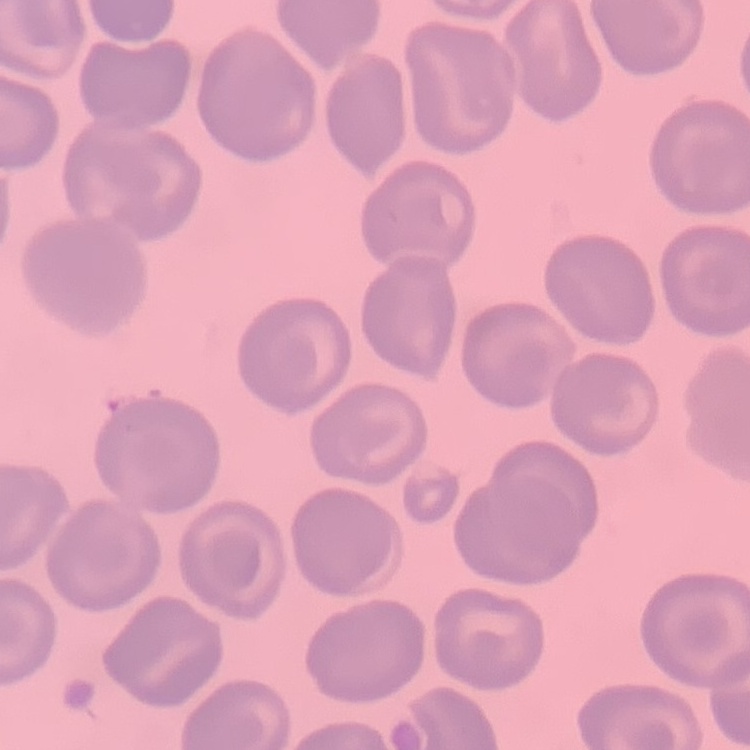
Summary:
  - Erythrocyte morphology: no rouleaux formation
  - Stain: Field's or Giemsa
  - Preparation: thin blood smear
  - Image type: square crop of a larger photomicrograph